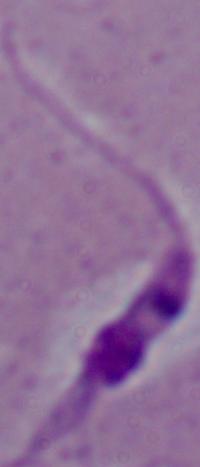
A Leishmania parasite is seen. Micrograph. 1000x magnification.